Describe the morphology of the red blood cells.
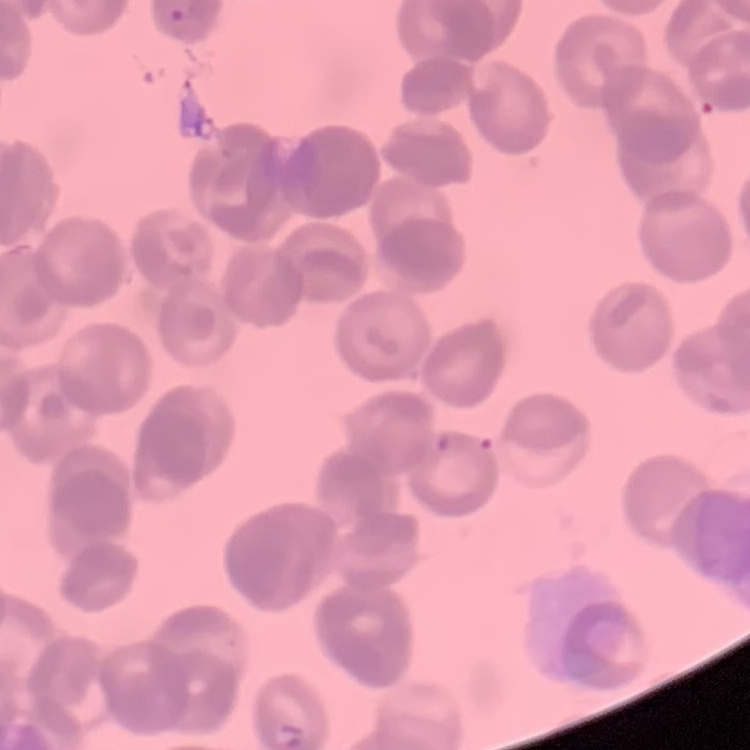
Rouleaux formation.

Summary:
  - Image type: square crop of a larger photomicrograph
  - Stain: Field's or Giemsa
  - Preparation: thin blood smear